Assess this cell for malaria.
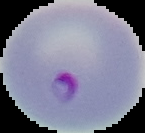

Parasitized.

From a thin blood smear. Segmented cell region on a black background. Image is 145×133 pixels.